Point out each Plasmodium parasite.
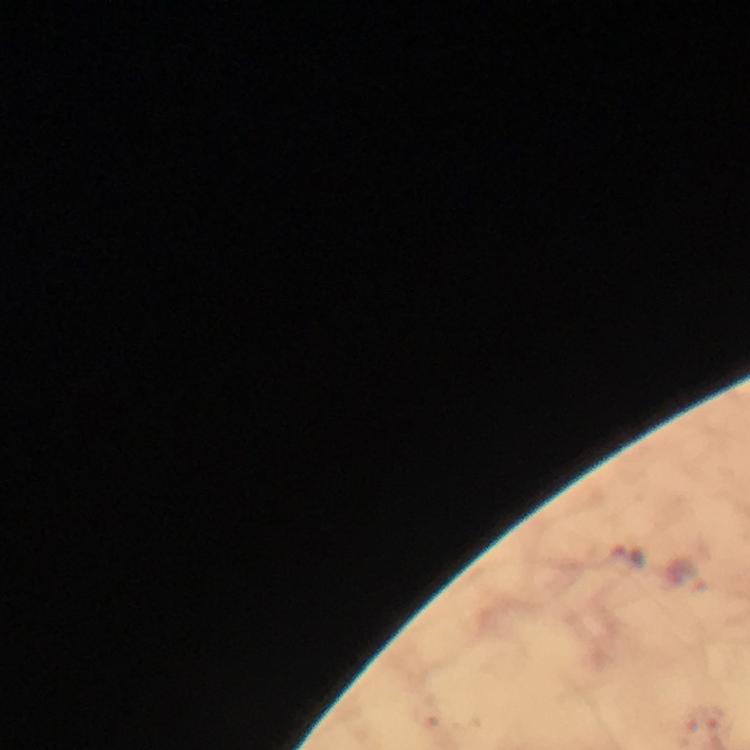
Approximate centers as [x, y] in pixels.
Plasmodium parasites: [627, 556].

From a malaria diagnostic workup. Thick blood smear. At 100x magnification. Image is 750×750 pixels. Immersion oil applied. Smartphone photograph taken through a microscope. Giemsa-stained preparation. A crop from one field of view.